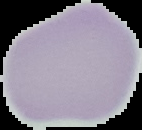
{
  "malaria_status": "uninfected",
  "image_size": "142×130 pixels",
  "preparation": "thin blood smear",
  "image_type": "segmented cell region with the area outside set to black"
}